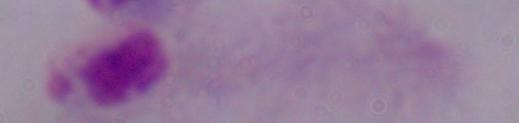 Captured at 1000x magnification. A trichomonad is seen. Photomicrograph.